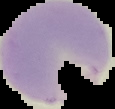

From a thin blood smear. Image is 115×109 pixels. Malaria status: parasitized. Cell region segmented out of the field of view; the surrounding area is masked to black.